Assess this cell for malaria.
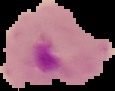
Parasitized.

preparation = thin blood film
image size = 115×91 pixels
image type = cell region segmented out of the field of view; surrounding area masked to black